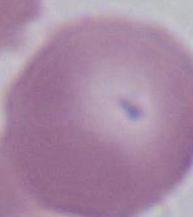

Photomicrograph. An erythrocyte is shown. 1000x magnification.